Identify the parasite.
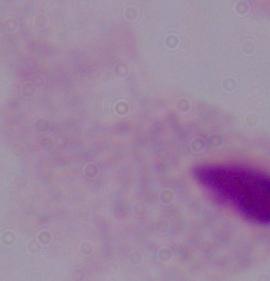

This is a trichomonad.

Summary:
  - Magnification: 1000x
  - Modality: photomicrograph